Report the malaria status of this cell.
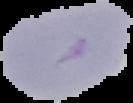
It is uninfected.

Summary:
  - Preparation: thin blood smear
  - Image type: segmented cell region with the area outside set to black
  - Image size: 133×103 pixels